Assess this cell for malaria.
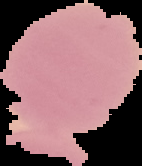

Uninfected.

Segmented cell region on a black background. From a thin blood smear. Image is 142×166 pixels.